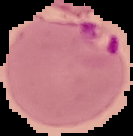
preparation: thin blood smear
image_size: 133×136 pixels
image_type: segmented cell region on a black background
malaria_status: parasitized